Assess this cell for malaria.
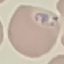

It is parasitized.

capture = smartphone camera at the microscope eyepiece
image type = cell patch, automatically extracted from a larger field of view and resized to 64 × 64 pixels
stain = Giemsa
preparation = thin blood film